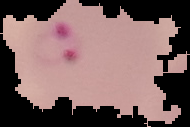
image_size: 190×127 pixels
image_type: segmented cell region with the area outside set to black
malaria_status: parasitized
preparation: thin blood film